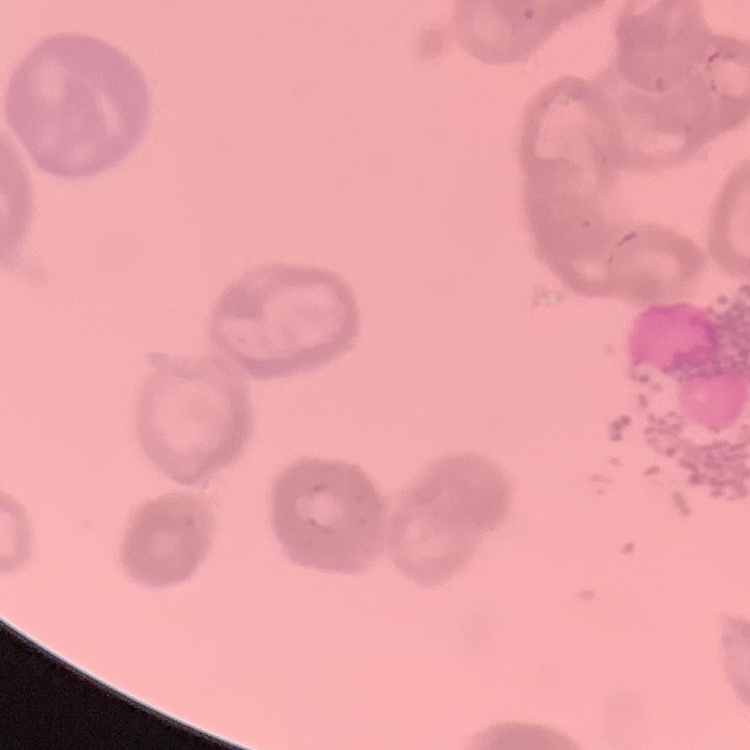

The erythrocytes show rouleaux formation. Square crop of a larger photomicrograph. Thin blood smear. Field's or Giemsa stain.